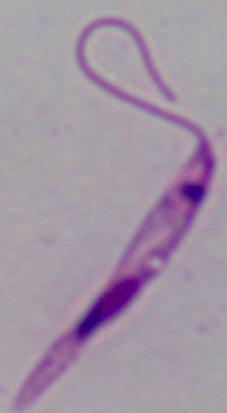 Captured at 1000x magnification. A Leishmania parasite is seen. Micrograph.